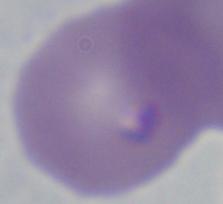

Micrograph. 1000x magnification. A Babesia parasite is seen.